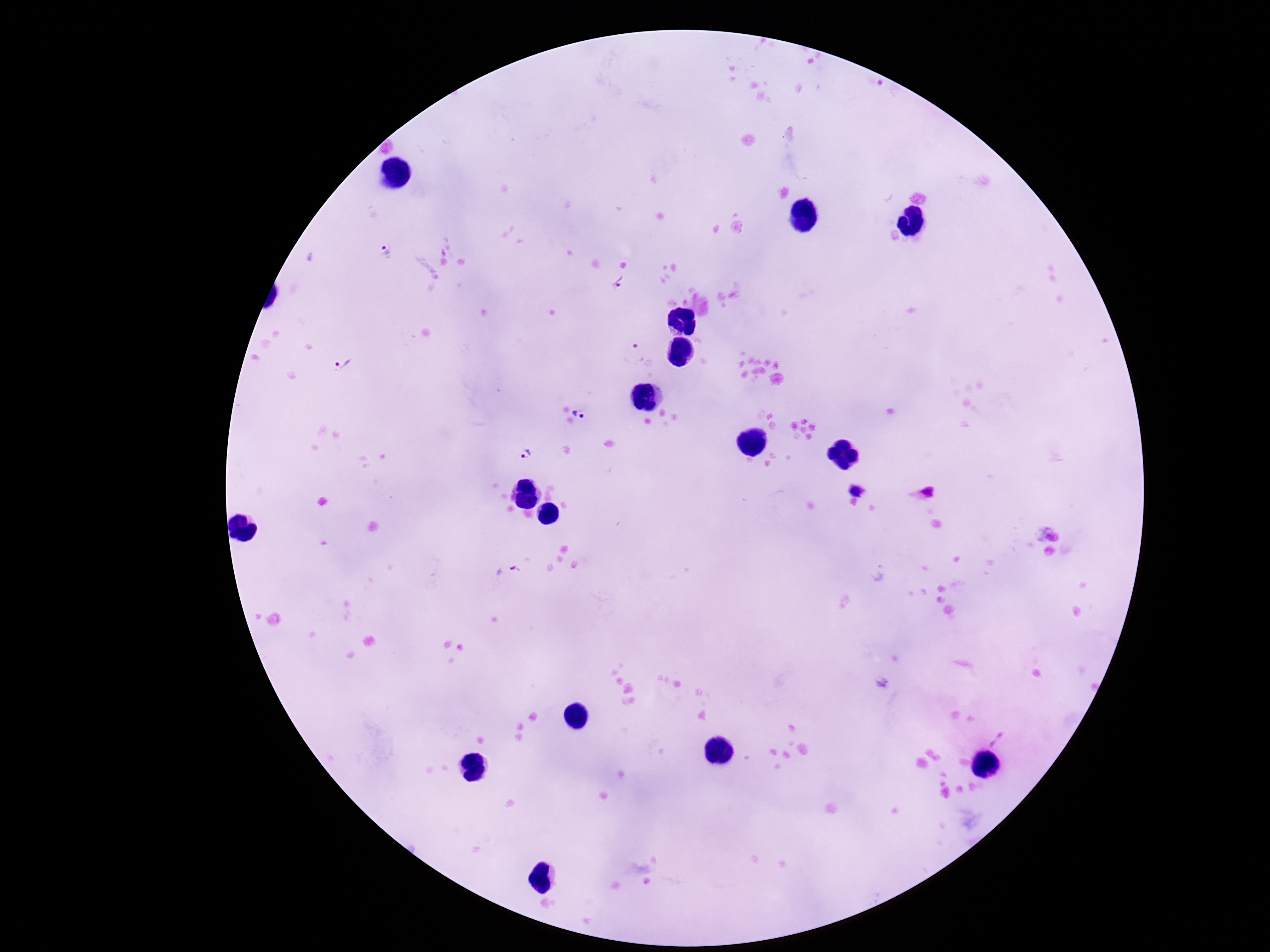

patient malaria status = infected
magnification = 100x
Plasmodium parasite locations = approximate centers as [x, y] in pixels: [386, 253], [618, 283], [631, 354], [340, 360], [581, 412], [526, 452], [856, 490], [922, 494], [1000, 740]
stain = Giemsa
image size = 1270×952 pixels
capture = smartphone camera through the microscope eyepiece
preparation = thick blood film
field of view = single